Report the malaria status of this cell.
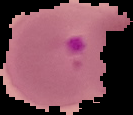

Parasitized.

Segmented cell region on a black background. Image is 133×115 pixels. From a thin blood smear.